Point out every Plasmodium parasite and every leukocyte.
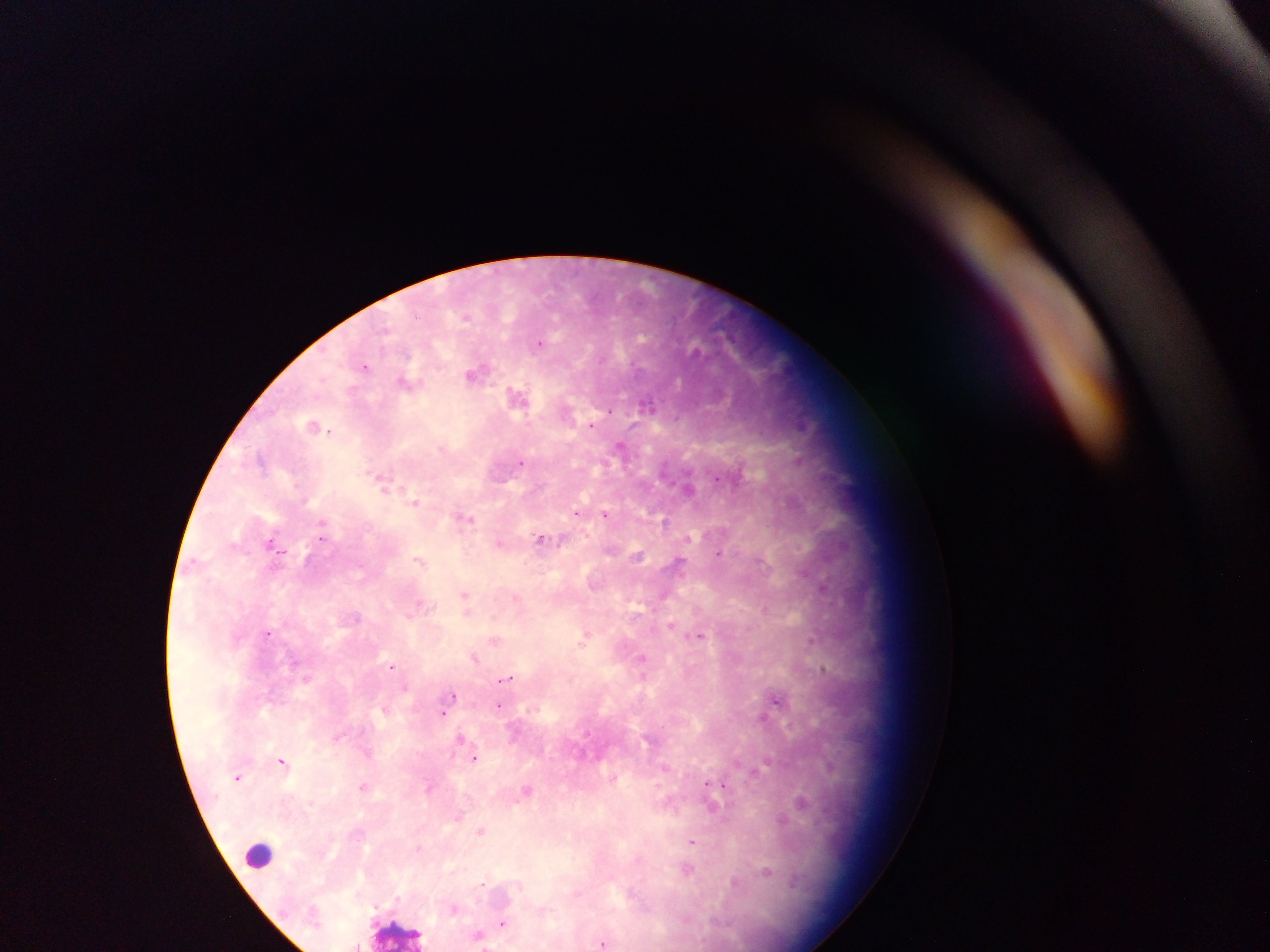
Approximate centers as x y in pixels.
Plasmodium parasites: 541 344; 364 366; 474 375; 592 424; 329 431; 520 463; 718 479; 579 511; 606 513; 663 520; 321 537; 542 538; 273 540; 720 552; 419 560; 765 608; 268 632; 700 635; 812 639; 583 643; 392 666; 823 668; 508 677; 455 695; 776 699; 498 704; 443 714; 475 757; 281 761; 237 779; 708 782; 362 786; 727 786; 693 843; 480 884; 502 924; 603 942.
Leukocytes: 259 857.

Image is 1270×952 pixels. Sample from Ghana. Thick blood film. One field of view. Photographed through a microscope with a mobile-phone camera.